Locate every uninfected red blood cell.
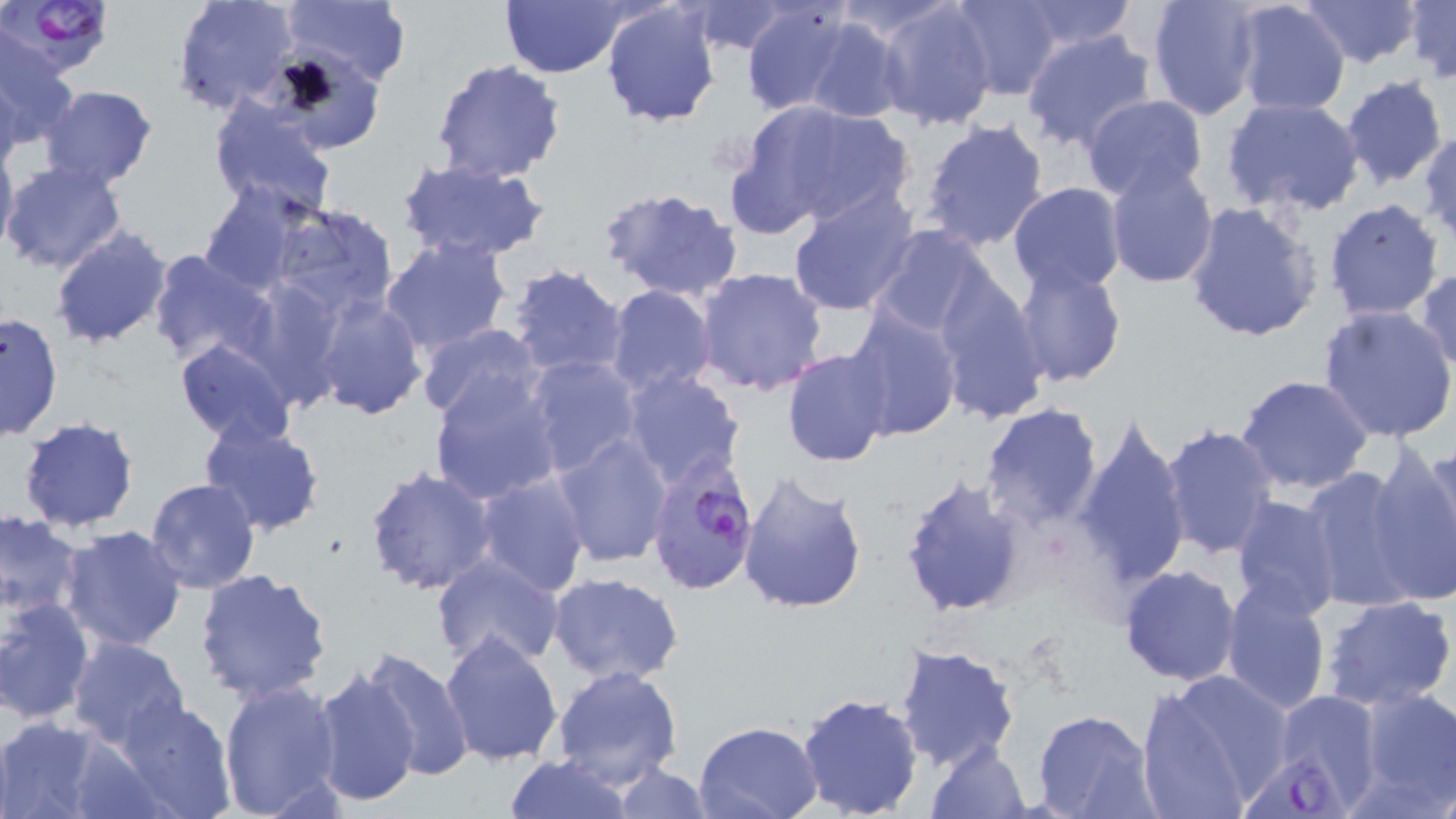
Approximate bounding boxes as (x1, y1, x2, y2) in pixels.
Uninfected red blood cells: (173, 0, 299, 116), (281, 0, 413, 88), (495, 0, 630, 77), (830, 0, 960, 43), (948, 0, 1063, 100), (1145, 0, 1263, 121), (1301, 0, 1421, 68), (1404, 0, 1454, 83), (740, 1, 856, 115), (875, 1, 1000, 130), (1012, 1, 1140, 54), (601, 2, 723, 126), (685, 2, 796, 55), (1229, 2, 1352, 117), (798, 18, 909, 124), (1021, 29, 1159, 152), (0, 35, 80, 150), (430, 58, 567, 185), (0, 72, 22, 182), (1338, 75, 1449, 189), (40, 85, 159, 190), (1080, 94, 1208, 202), (1222, 95, 1365, 218), (207, 97, 337, 218), (735, 99, 914, 233), (919, 117, 1051, 251), (1420, 129, 1456, 244), (0, 137, 19, 266), (1104, 158, 1216, 287), (1, 159, 127, 275), (397, 159, 550, 262), (1008, 181, 1126, 295), (198, 182, 307, 296), (599, 185, 743, 303), (788, 186, 921, 316), (1324, 198, 1444, 319), (1184, 200, 1323, 343), (268, 204, 399, 321), (866, 223, 1008, 350), (50, 226, 172, 348), (379, 235, 513, 356), (146, 246, 275, 368), (1012, 260, 1126, 387), (506, 263, 629, 379), (694, 267, 828, 395), (1413, 268, 1456, 375), (931, 271, 1050, 426), (605, 284, 719, 398), (312, 292, 428, 421), (843, 304, 962, 441), (1317, 305, 1456, 444), (1, 311, 64, 442), (414, 323, 548, 425), (174, 338, 297, 447), (782, 347, 891, 468), (523, 355, 644, 478), (428, 369, 564, 502), (620, 369, 747, 492), (1234, 375, 1375, 494), (979, 403, 1104, 528), (1074, 414, 1193, 593), (16, 416, 140, 534), (198, 420, 327, 537), (1160, 423, 1278, 561), (550, 433, 673, 566), (1364, 446, 1456, 606), (1300, 463, 1425, 614), (365, 465, 495, 595), (737, 470, 869, 616), (474, 472, 590, 598), (897, 474, 1029, 617), (145, 477, 261, 594), (1229, 495, 1343, 620), (0, 511, 85, 620), (57, 524, 188, 651), (429, 554, 567, 672), (1119, 566, 1242, 686), (194, 568, 332, 704), (545, 572, 685, 685), (1220, 581, 1331, 713), (1322, 595, 1456, 710), (0, 596, 96, 725), (439, 629, 564, 766), (67, 636, 191, 751), (358, 644, 473, 778), (895, 644, 1020, 770), (551, 663, 684, 791), (310, 665, 424, 806), (1133, 673, 1280, 819), (218, 680, 346, 819), (1351, 687, 1456, 813), (795, 691, 925, 819), (1267, 692, 1385, 812), (115, 697, 238, 819), (1033, 711, 1160, 819), (0, 716, 109, 819), (692, 720, 824, 819), (64, 736, 176, 819), (926, 741, 1032, 818), (503, 753, 632, 819), (611, 763, 710, 819).

Summary:
  - Plasmodium falciparum-infected red blood cell locations: (5, 0, 116, 79), (644, 451, 760, 594), (1244, 743, 1365, 819)
  - Slide-level diagnosis: Plasmodium falciparum
  - Image size: 1456×819 pixels
  - Field of view: single
  - Magnification: 1000x
  - Preparation: thin blood smear
  - Modality: optical microscopy
  - Stain: May-Grünwald-Giemsa